Report the malaria status of this cell.
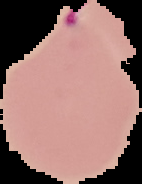
It is parasitized.

{
  "image_size": "142×184 pixels",
  "preparation": "thin blood smear",
  "image_type": "segmented cell region on a black background"
}